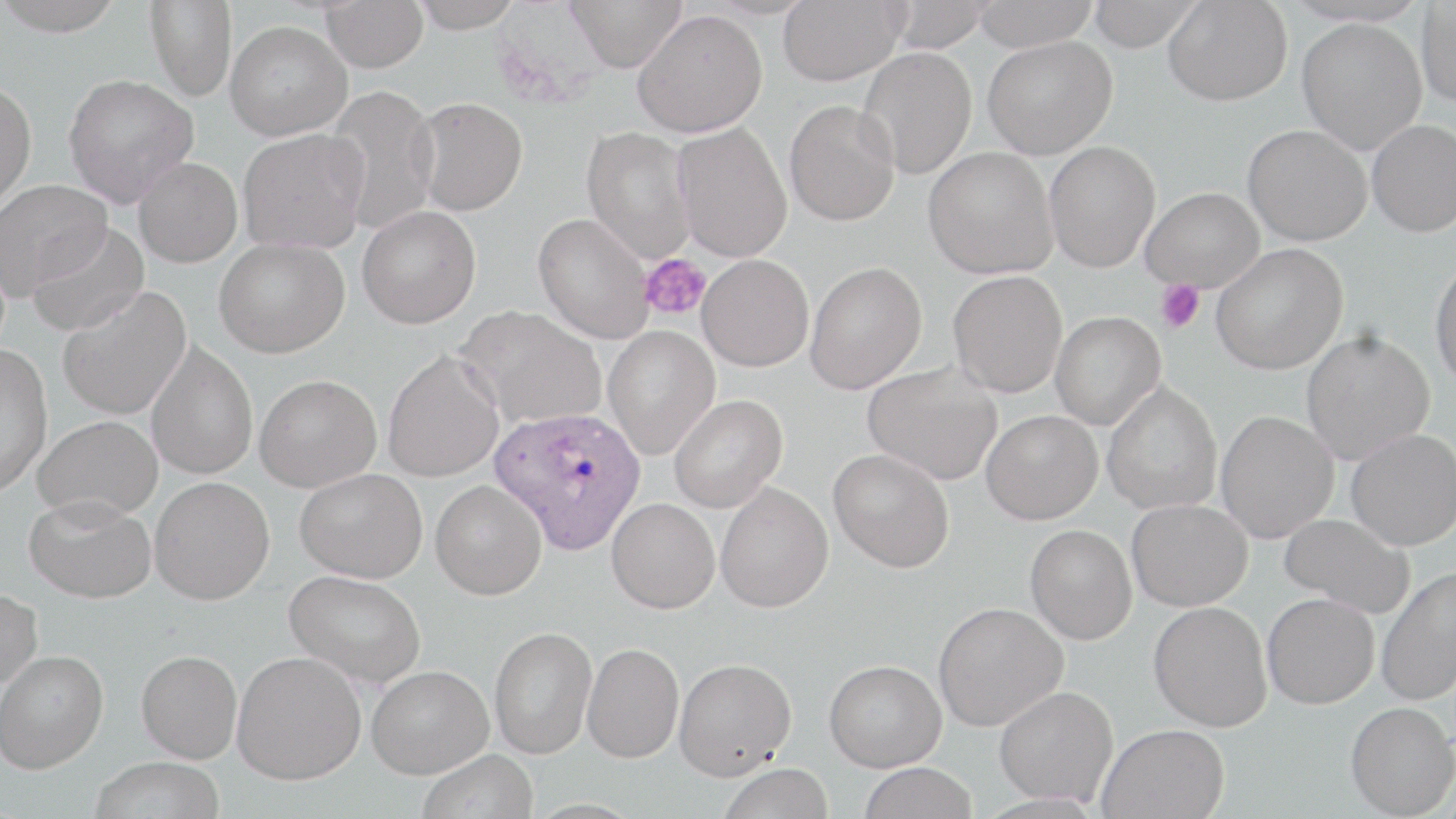

Summary:
  - Coordinate format: approximate bounding boxes as [x1, y1, x2, y2] in pixels
  - Plasmodium ovale-infected red blood cell locations: [488, 405, 648, 555]
  - Platelet locations: [639, 253, 711, 321], [1154, 280, 1205, 333]
  - Uninfected red blood cell locations: [0, 0, 128, 35], [145, 0, 237, 101], [320, 0, 429, 72], [410, 0, 525, 32], [565, 0, 688, 72], [777, 0, 907, 85], [883, 0, 994, 52], [971, 0, 1099, 52], [1086, 0, 1203, 51], [1163, 1, 1293, 106], [1416, 2, 1456, 108], [632, 8, 768, 137], [1297, 18, 1427, 154], [224, 20, 351, 141], [982, 35, 1117, 159], [857, 47, 977, 179], [63, 73, 199, 208], [0, 80, 37, 213], [323, 85, 441, 233], [412, 97, 529, 216], [783, 100, 901, 227], [1366, 119, 1456, 237], [673, 122, 793, 263], [1243, 124, 1372, 246], [581, 127, 697, 264], [238, 128, 369, 254], [1043, 141, 1161, 272], [923, 146, 1058, 279], [133, 156, 242, 267], [0, 179, 112, 297], [1140, 187, 1264, 292], [357, 206, 481, 329], [533, 213, 653, 344], [26, 222, 150, 336], [213, 237, 350, 358], [1210, 243, 1348, 374], [697, 254, 815, 371], [1430, 257, 1456, 391], [804, 262, 927, 394], [948, 271, 1068, 398], [57, 285, 192, 420], [456, 305, 607, 428], [1050, 311, 1166, 430], [603, 326, 720, 459], [1300, 328, 1435, 465], [146, 340, 258, 480], [0, 343, 53, 498], [382, 349, 504, 482], [863, 361, 1003, 485], [255, 374, 381, 492], [1102, 382, 1222, 515], [669, 394, 787, 513], [981, 410, 1103, 524], [1216, 410, 1339, 543], [32, 414, 162, 522], [1346, 429, 1456, 551], [828, 449, 955, 572], [295, 468, 427, 583], [150, 476, 275, 604], [430, 480, 547, 600], [715, 482, 834, 613], [24, 495, 156, 603], [606, 498, 720, 613], [1127, 499, 1253, 611], [1279, 513, 1416, 619], [1025, 525, 1137, 644], [1375, 565, 1456, 706], [284, 569, 426, 688], [0, 587, 43, 693], [1262, 592, 1380, 709], [932, 601, 1068, 731], [1149, 601, 1272, 731], [489, 626, 598, 758], [582, 642, 684, 763], [0, 650, 108, 773], [136, 650, 242, 763], [232, 650, 366, 784], [674, 658, 797, 778], [824, 659, 947, 771], [367, 665, 493, 778], [994, 685, 1119, 807], [1345, 701, 1456, 818], [1098, 723, 1229, 819], [417, 748, 538, 819], [88, 756, 225, 818], [858, 762, 978, 818], [718, 763, 834, 819]
  - Slide-level diagnosis: Plasmodium ovale
  - Preparation: thin blood film
  - Image size: 1456×819 pixels
  - Modality: optical microscopy
  - Stain: May-Grünwald-Giemsa
  - Magnification: 1000x
  - Field of view: one of a larger specimen